Point out each Plasmodium parasite.
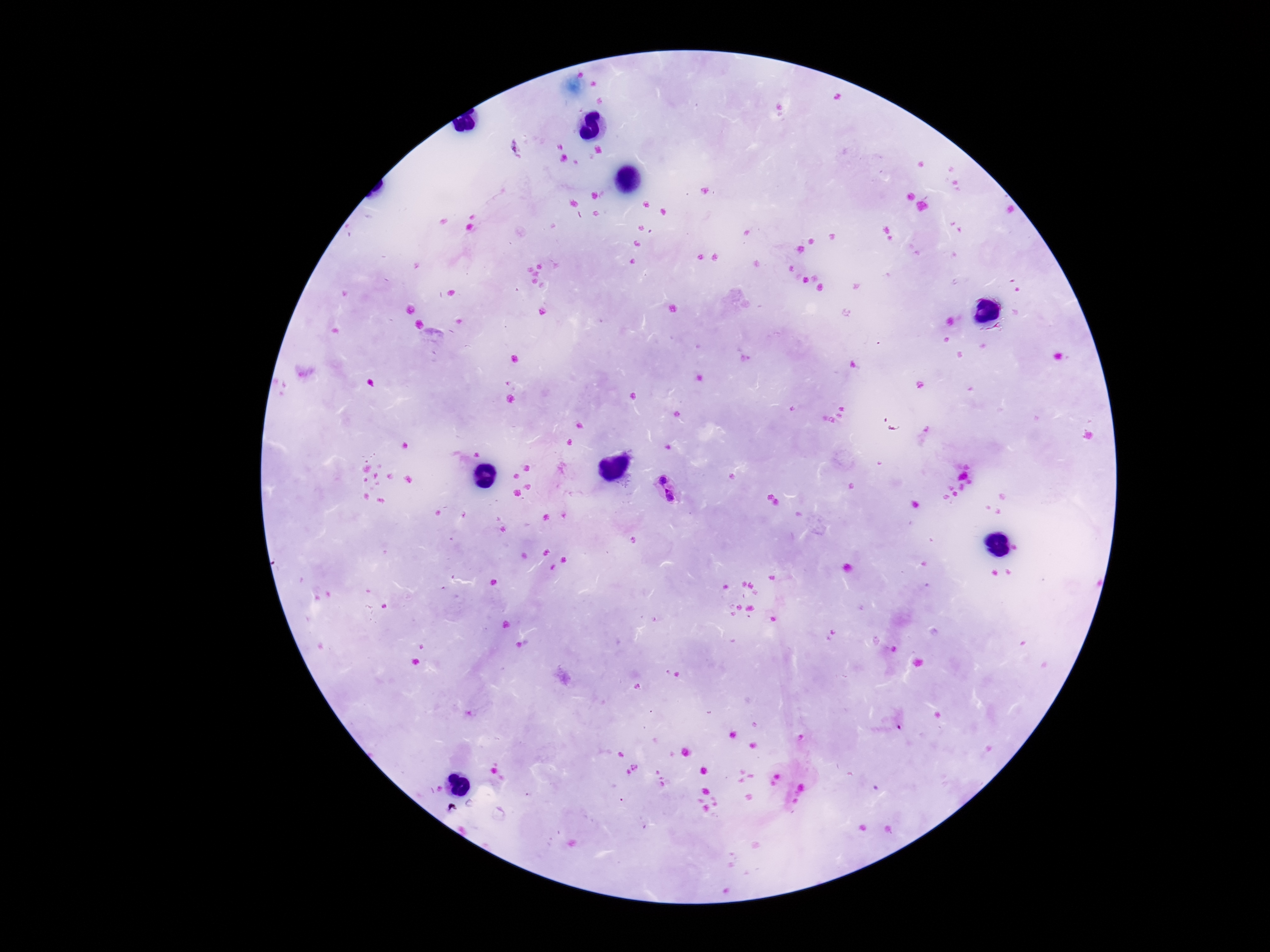

Approximate centers as (x, y) in pixels.
Plasmodium parasites: (514, 148), (661, 479), (671, 496).

Summary:
  - Capture: smartphone camera through the microscope eyepiece
  - Preparation: thick blood film
  - Field of view: one from this slide
  - Stain: Giemsa
  - Magnification: 100x
  - Image size: 1270×952 pixels
  - Patient malaria status: infected